Describe the morphology of the erythrocytes.
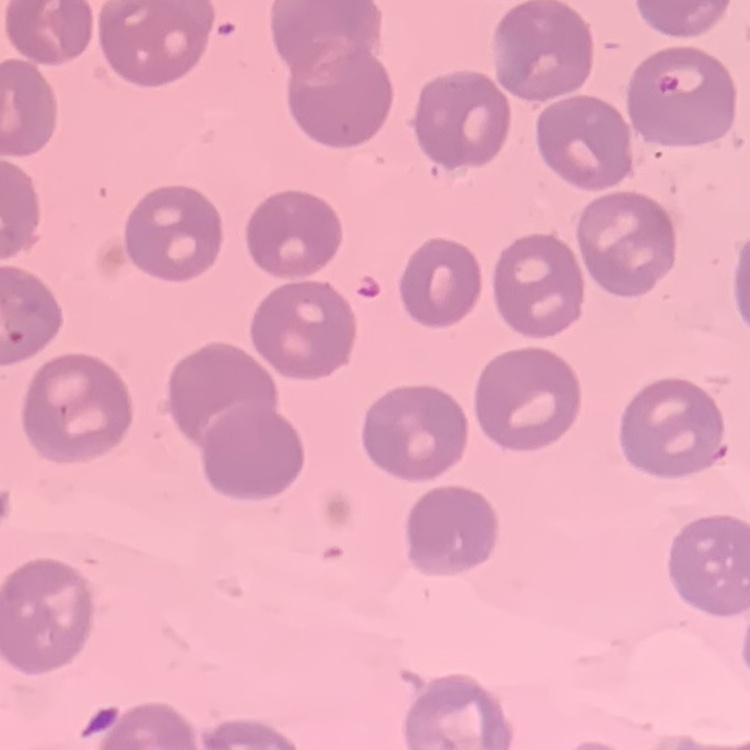

No rouleaux formation.

preparation = thin blood film
stain = Field's or Giemsa
image type = square crop of a larger photomicrograph